Locate every Plasmodium parasite.
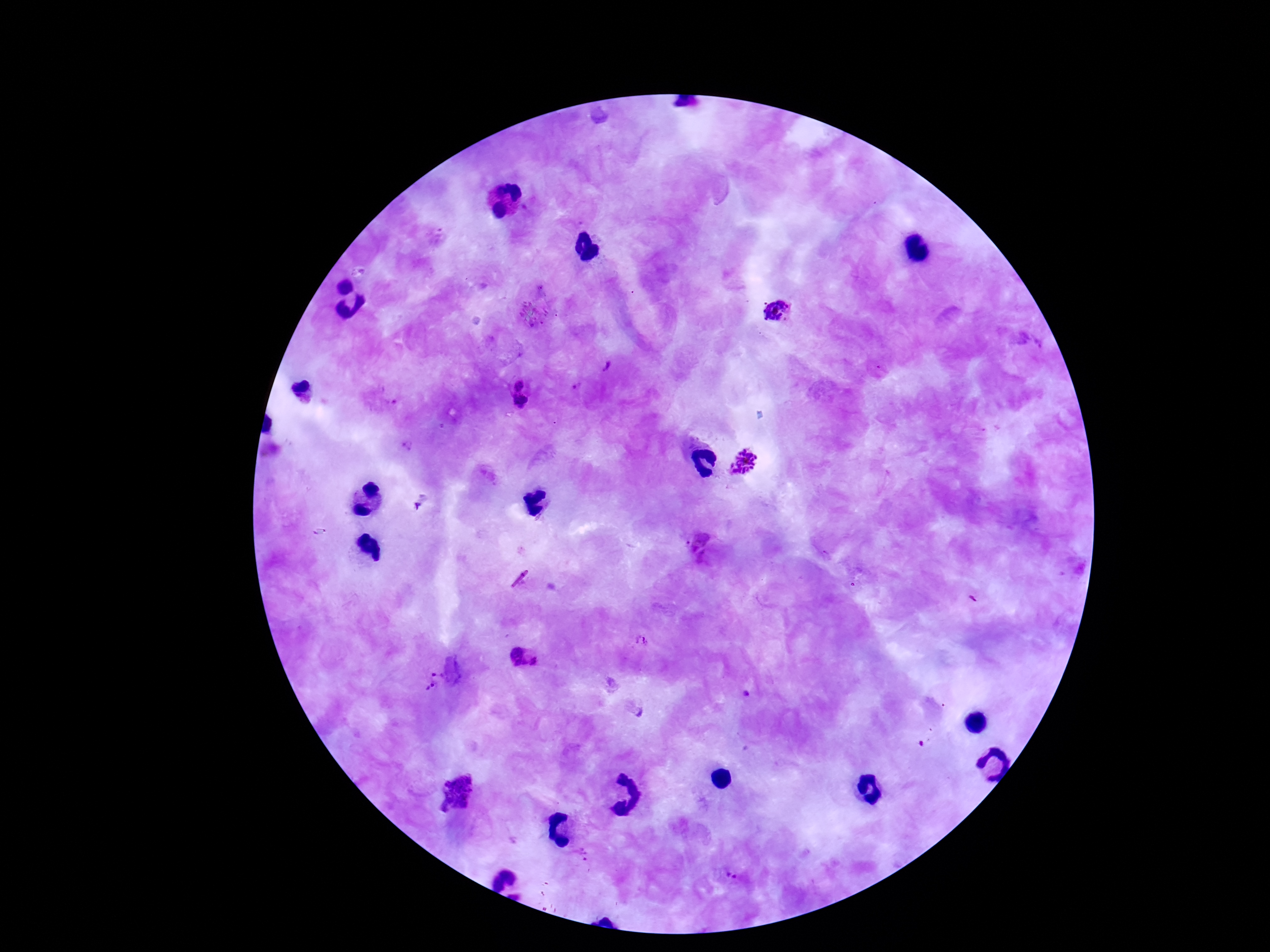
Approximate object centers, in pixels from the top-left corner.
Plasmodium parasites: (x=776, y=312), (x=608, y=366), (x=518, y=382), (x=577, y=385), (x=520, y=403), (x=407, y=447), (x=746, y=463), (x=700, y=544), (x=826, y=555), (x=971, y=599), (x=640, y=640), (x=515, y=657), (x=537, y=662), (x=432, y=680), (x=637, y=708), (x=921, y=744), (x=456, y=792), (x=580, y=854), (x=731, y=876).

100x magnification. Giemsa stain. Patient malaria status: infected. Thick blood smear. Single field of view. Photographed through the microscope eyepiece with a smartphone camera. Image is 1270×952 pixels.